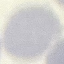
Summary:
  - Result: no malaria parasites detected
  - Capture: smartphone camera at the microscope eyepiece
  - Stain: Giemsa
  - Preparation: thin smear
  - Image type: automatically extracted cell patch, resized to 64 × 64 pixels